Report the malaria status of this cell.
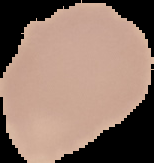
Uninfected.

Summary:
  - Image size: 154×163 pixels
  - Preparation: thin blood film
  - Image type: cell region segmented out of the field of view; surrounding area masked to black